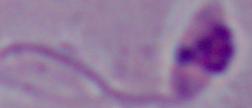
Captured at 1000x magnification. Micrograph. A Leishmania parasite is shown.